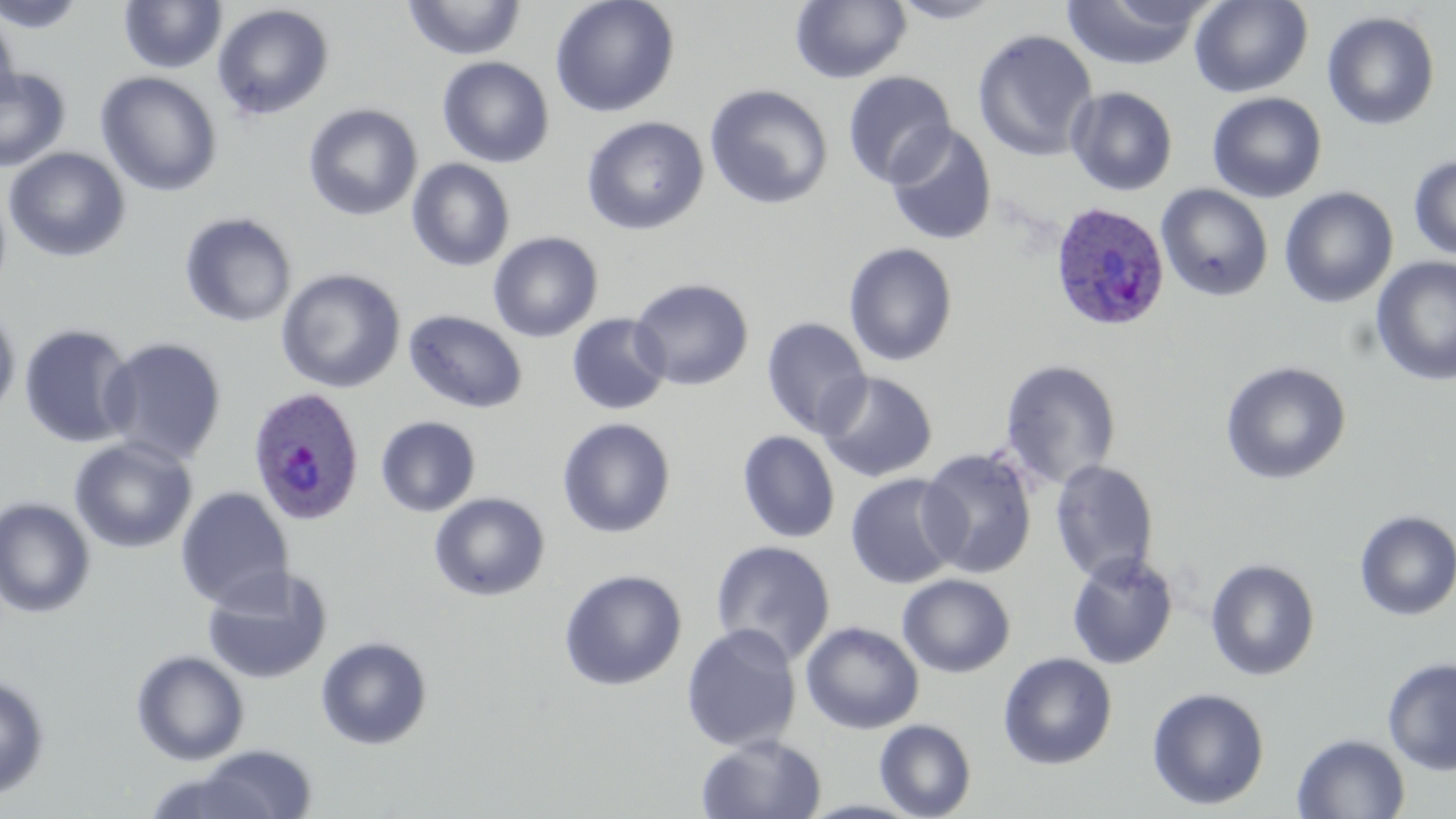
Approximate bounding boxes as [x1, y1, x2, y2] in pixels. Uninfected red blood cell locations: [0, 0, 87, 33], [118, 0, 227, 74], [549, 0, 680, 118], [790, 0, 912, 84], [887, 0, 1008, 24], [1061, 0, 1209, 71], [1189, 0, 1313, 98], [403, 1, 526, 61], [211, 3, 335, 121], [0, 7, 21, 112], [1321, 10, 1440, 131], [972, 29, 1098, 162], [438, 57, 555, 168], [1, 67, 70, 173], [95, 71, 223, 197], [842, 71, 957, 188], [704, 84, 833, 210], [1066, 86, 1178, 196], [1207, 92, 1327, 203], [303, 103, 423, 221], [581, 116, 709, 236], [884, 124, 997, 245], [3, 147, 131, 262], [1408, 155, 1456, 262], [406, 159, 515, 272], [1156, 184, 1273, 301], [1279, 186, 1398, 308], [179, 211, 297, 328], [488, 232, 603, 342], [843, 242, 958, 367], [1370, 256, 1456, 386], [275, 268, 406, 393], [629, 277, 754, 391], [0, 303, 21, 424], [404, 310, 528, 414], [566, 313, 671, 415], [760, 316, 872, 438], [19, 323, 138, 448], [99, 336, 228, 466], [999, 359, 1121, 490], [1220, 360, 1352, 485], [815, 371, 938, 483], [375, 415, 481, 517], [557, 417, 676, 538], [737, 430, 840, 543], [69, 437, 198, 554], [917, 447, 1038, 579], [1050, 460, 1159, 585], [845, 472, 963, 590], [175, 486, 294, 612], [429, 491, 550, 602], [0, 497, 96, 618], [1354, 510, 1456, 621], [709, 540, 836, 665], [1066, 552, 1179, 670], [1205, 558, 1320, 681], [202, 566, 335, 684], [558, 569, 688, 691], [897, 573, 1016, 678], [800, 620, 924, 734], [681, 624, 802, 752], [316, 635, 433, 750], [131, 649, 250, 766], [998, 652, 1118, 770], [1382, 657, 1456, 775], [0, 672, 51, 800], [1146, 686, 1270, 811], [874, 718, 977, 819], [696, 733, 827, 819], [1291, 733, 1410, 818], [190, 743, 317, 818]. Plasmodium ovale-infected red blood cell locations: [1049, 202, 1170, 332], [247, 386, 366, 526]. Slide-level diagnosis: Plasmodium ovale. Image is 1456×819 pixels. May-Grünwald-Giemsa stain. Light microscopy. Single field of view. Thin blood film. Captured at 1000x magnification.